Outline each P. falciparum parasite and classify it by life-cycle stage.
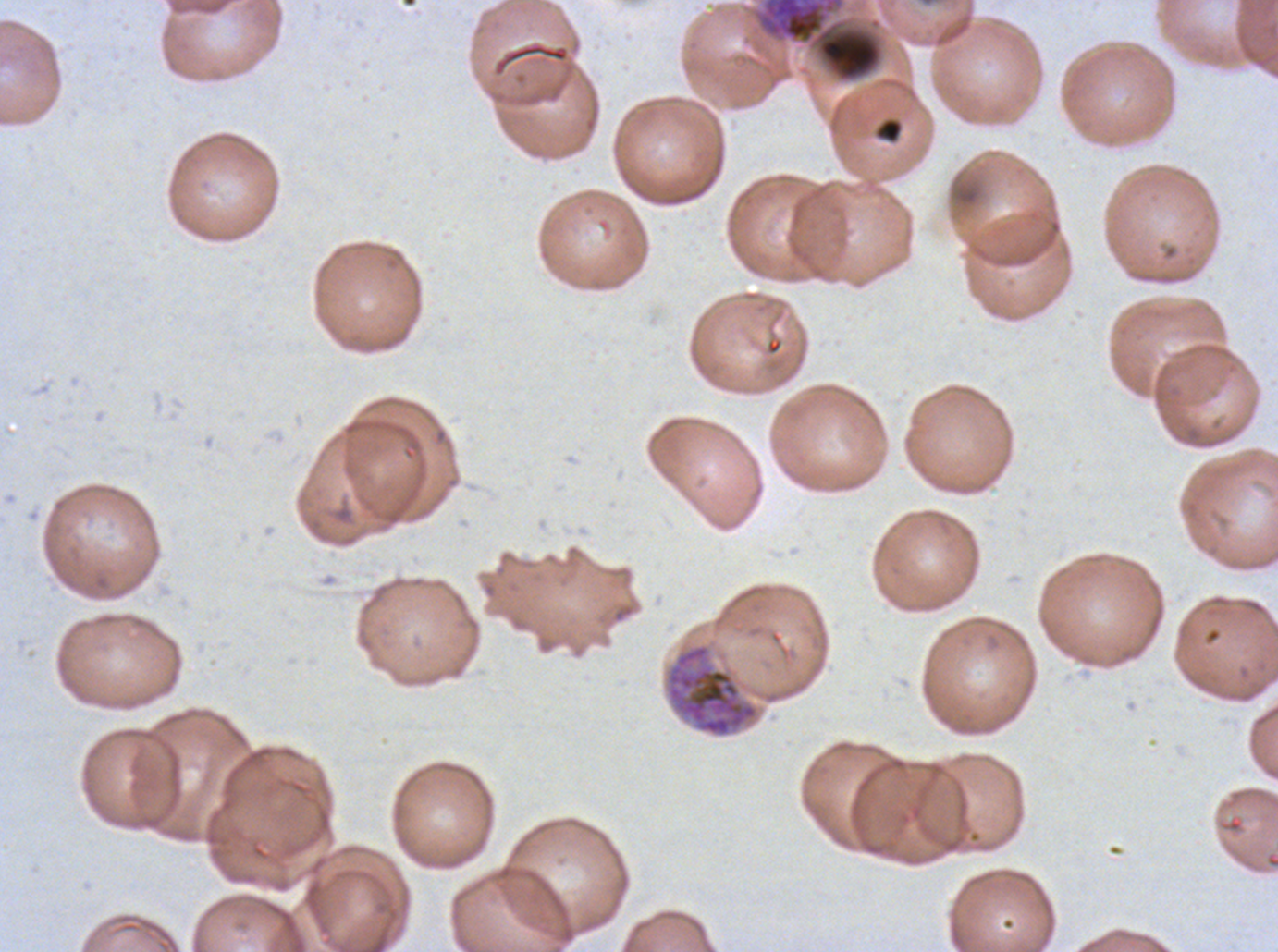

Approximate bounding boxes as [x1, y1, x2, y2] in pixels.
Early schizonts: [666, 643, 759, 738].
No rings, late-ring/early-trophozoite forms, mid trophozoites, late trophozoites, late schizonts, segmenters, or gametocytes observed.

Debris locations: [758, 0, 883, 82], [875, 117, 903, 143]. Thin blood smear. A sub-image separated from a larger composite. Giemsa stain. P. falciparum from a patient in The Gambia, cultured ex vivo for 24 to 48 hours. Image is 1278×952 pixels.